Outline each Plasmodium ovale-infected red blood cell.
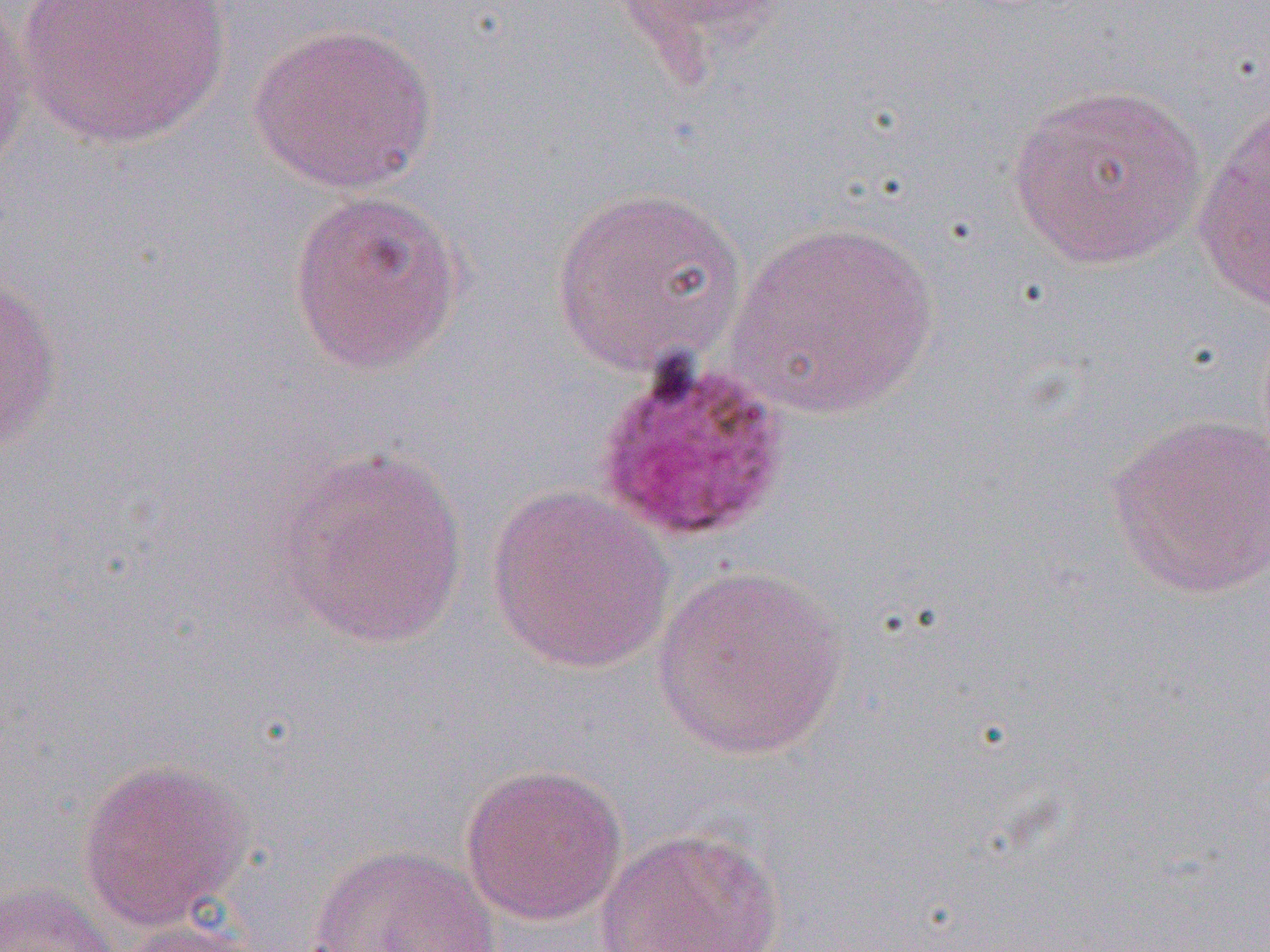
Approximate bounding boxes as (x1,y1)-(x2,y2) corner pairs in pixels.
Plasmodium ovale-infected red blood cells: (591,351)-(794,547).

Summary:
  - Uninfected red blood cell locations: (10,0)-(235,152), (0,1)-(36,182), (249,21)-(437,194), (1007,81)-(1208,271), (1191,99)-(1269,314), (551,185)-(750,376), (286,187)-(466,376), (723,219)-(942,419), (0,268)-(64,458), (1105,413)-(1270,600), (273,445)-(470,653), (486,484)-(675,674), (651,563)-(851,762), (75,757)-(252,933), (459,763)-(627,926), (596,827)-(788,951), (307,845)-(500,952), (0,881)-(120,952), (108,919)-(272,952)
  - Slide-level diagnosis: Plasmodium ovale
  - Modality: light microscopy
  - Image size: 1270×952 pixels
  - Magnification: 1000x
  - Preparation: thin blood film
  - Field of view: single